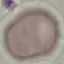

{
  "result": "negative for malaria parasites",
  "capture": "smartphone through the microscope eyepiece",
  "image_type": "cell patch, automatically extracted from a larger field of view and resized to 64 × 64 pixels",
  "stain": "Giemsa",
  "preparation": "thin smear"
}